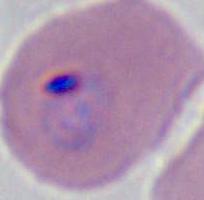

Summary:
  - Modality: micrograph
  - Identification: Plasmodium
  - Magnification: 400x or 1000x